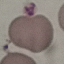
Summary:
  - Result: no malaria parasites detected
  - Preparation: thin smear
  - Capture: smartphone camera at the microscope eyepiece
  - Image type: cell patch, automatically extracted from a larger field of view and resized to 64 × 64 pixels
  - Stain: Giemsa